State the preparation type.
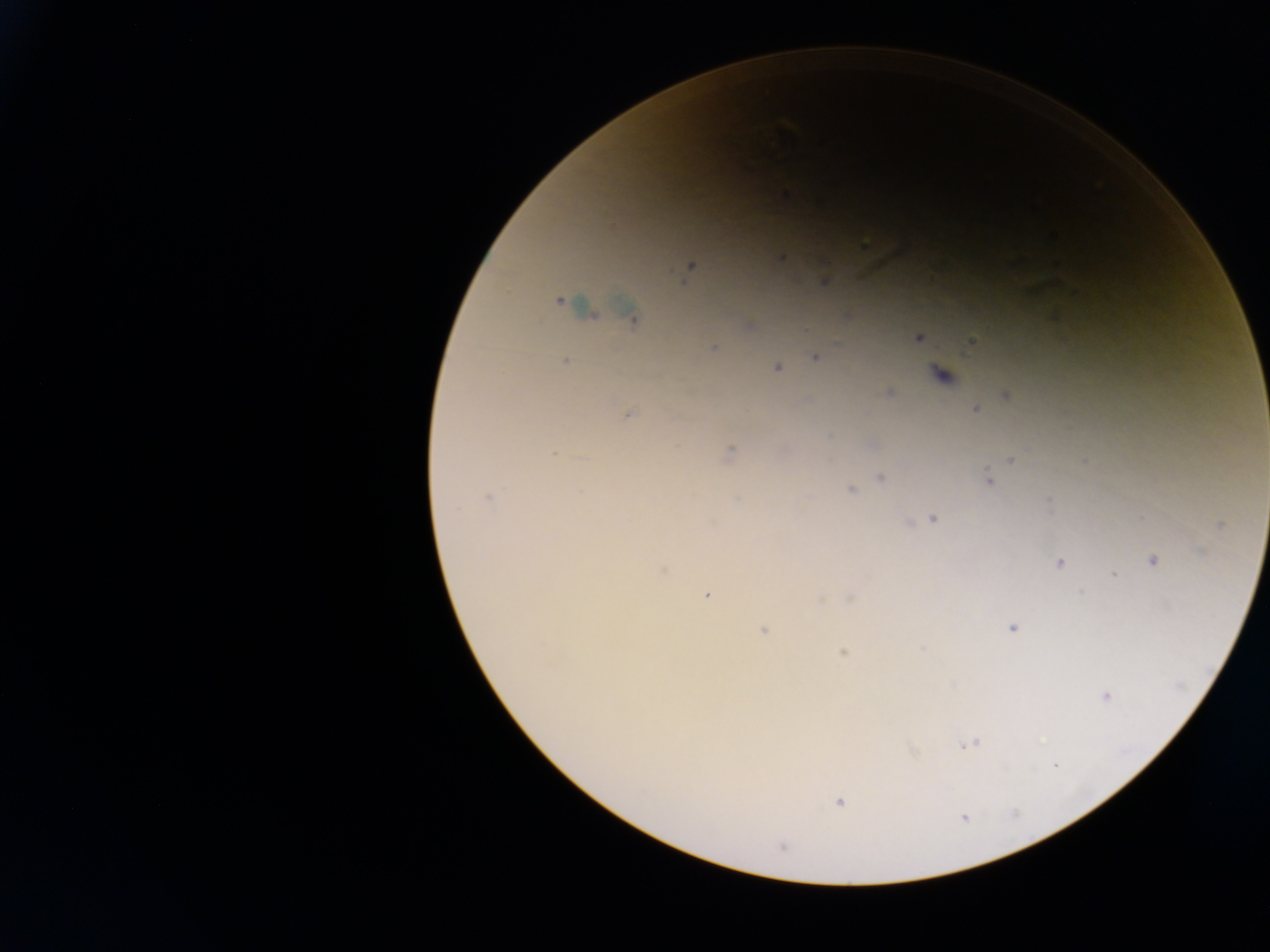

Thick blood smear.

image size = 1270×952 pixels
Plasmodium parasite locations = approximate centers as {x, y} in pixels: {783, 194}, {1051, 236}, {863, 241}, {780, 257}, {690, 266}, {824, 280}, {558, 300}, {589, 311}, {632, 319}, {917, 338}, {972, 341}, {714, 347}, {815, 356}, {565, 361}, {777, 367}, {941, 375}, {889, 391}, {1006, 395}, {975, 409}, {628, 414}, {730, 452}, {1013, 459}, {881, 478}, {989, 480}, {851, 490}, {487, 497}, {932, 518}, {908, 521}, {1220, 525}, {1154, 560}, {1058, 563}, {662, 568}, {1114, 575}, {707, 595}, {852, 598}, {1011, 627}, {763, 629}, {844, 653}, {1105, 695}, {968, 744}, {838, 802}, {964, 818}
capture = mobile-phone photograph through a microscope
field of view = single
country = Ghana